Assess this cell for malaria.
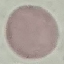

It is uninfected.

stain: Giemsa
capture: smartphone through the microscope eyepiece
image_type: cell patch, automatically extracted from a larger field of view and resized to 64 × 64 pixels
preparation: thin blood smear